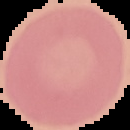
Segmented cell region on a black background. Image is 130×130 pixels. Result: negative for Plasmodium parasites. From a thin blood smear.